Describe the morphology of the red blood cells.
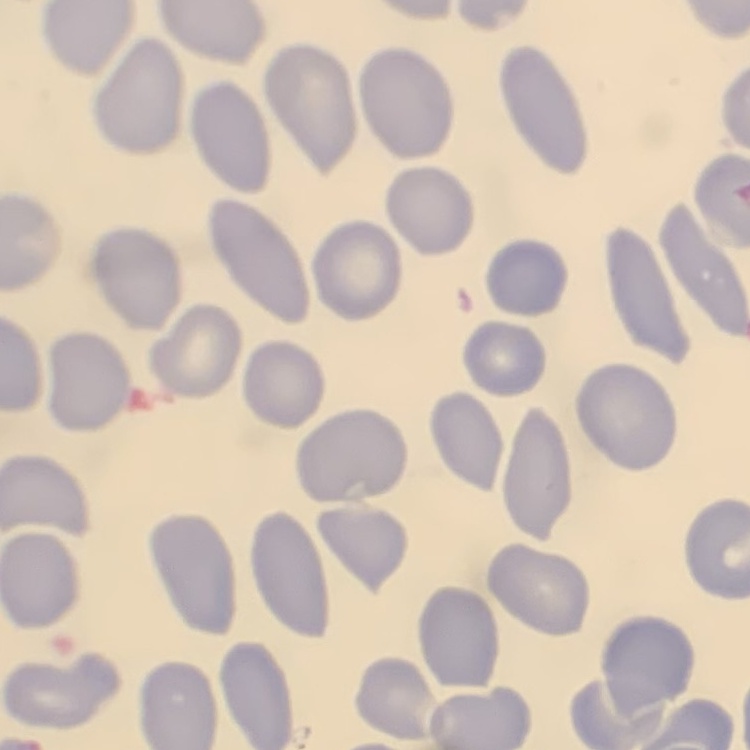
They show no rouleaux formation.

Field's or Giemsa stain. Square crop of a larger photomicrograph. Thin blood smear.